Assess this cell for malaria.
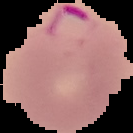
It is parasitized.

Segmented cell region on a black background. Image is 133×133 pixels. From a thin blood film.